State which cell type is depicted.
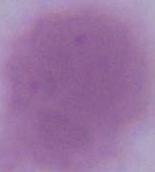
An erythrocyte.

magnification: 1000x
modality: micrograph